Locate every leukocyte (white blood cell).
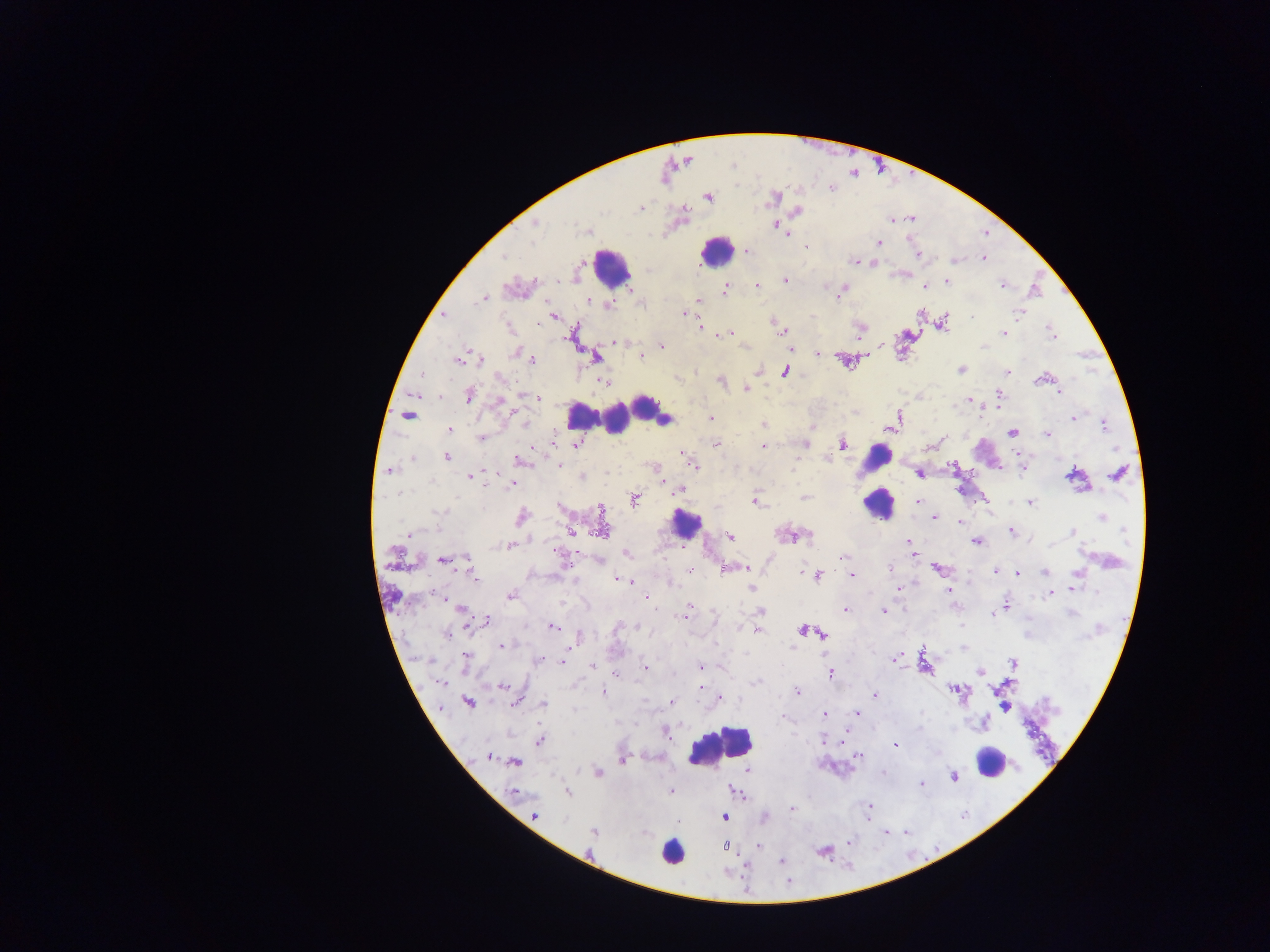

Approximate centers as x y in pixels.
Leukocytes: 718 252; 607 264; 619 408; 872 478; 684 531; 721 746; 993 761; 672 853.

Malaria parasite locations: 775 196; 708 197; 797 211; 775 226; 790 233; 877 243; 805 248; 748 250; 983 258; 857 261; 954 262; 875 264; 785 280; 948 282; 756 285; 1002 285; 727 288; 924 288; 841 294; 482 298; 837 298; 589 299; 697 299; 593 302; 607 305; 685 313; 972 314; 444 315; 1018 316; 944 320; 538 324; 702 326; 776 327; 730 331; 1003 332; 722 335; 1052 336; 614 343; 661 345; 981 345; 880 349; 817 354; 512 355; 640 356; 596 359; 532 360; 456 361; 961 370; 784 372; 1007 372; 422 374; 721 381; 603 383; 745 388; 1059 392; 468 394; 999 394; 438 395; 521 395; 499 399; 536 401; 973 401; 985 411; 710 417; 1072 419; 525 423; 763 424; 1104 424; 447 430; 1047 433; 1012 434; 554 436; 941 440; 481 441; 716 443; 805 445; 532 446; 574 446; 843 446; 764 447; 931 448; 1116 449; 681 455; 448 458; 518 461; 558 465; 694 466; 951 466; 388 471; 607 473; 919 473; 1117 473; 580 476; 470 478; 431 481; 662 483; 512 484; 487 487; 678 491; 401 495; 804 496; 754 503; 918 503; 1028 503; 990 509; 437 512; 442 513; 521 515; 1102 518; 933 519; 960 523; 1125 532; 409 533; 572 533; 1073 533; 1013 535; 731 536; 808 536; 909 543; 977 543; 513 544; 1051 544; 555 548; 625 555; 844 558; 441 562; 468 563; 745 567; 890 567; 935 568; 994 571; 1044 574; 1075 574; 1018 575; 818 576; 851 576; 473 579; 615 579; 897 590; 948 591; 1072 591; 510 596; 1049 596; 646 600; 1006 602; 458 606; 687 607; 845 609; 760 611; 883 611; 685 612; 992 615; 488 619; 466 626; 554 626; 636 626; 757 630; 443 637; 572 645; 500 646; 792 647; 789 648; 464 657; 892 658; 539 661; 560 662; 591 665; 703 666; 644 669; 979 671; 830 673; 617 674; 756 683; 443 685; 958 686; 701 687; 604 693; 797 693; 875 695; 720 696; 671 702; 468 703; 514 703; 543 703; 859 714; 824 715; 538 740; 823 741; 894 745; 487 756; 857 756; 622 761; 514 763; 598 772; 921 784; 671 790; 869 805; 867 809; 790 810; 535 816; 725 817; 884 833; 593 834; 847 840; 759 845; 824 853; 781 862. One field of view. Thick blood smear. Image is 1270×952 pixels. Photographed through a microscope with a mobile-phone camera. Sample from Ghana.